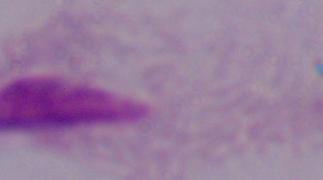
Micrograph. A trichomonad is seen. Captured at 1000x magnification.